Find each WBC.
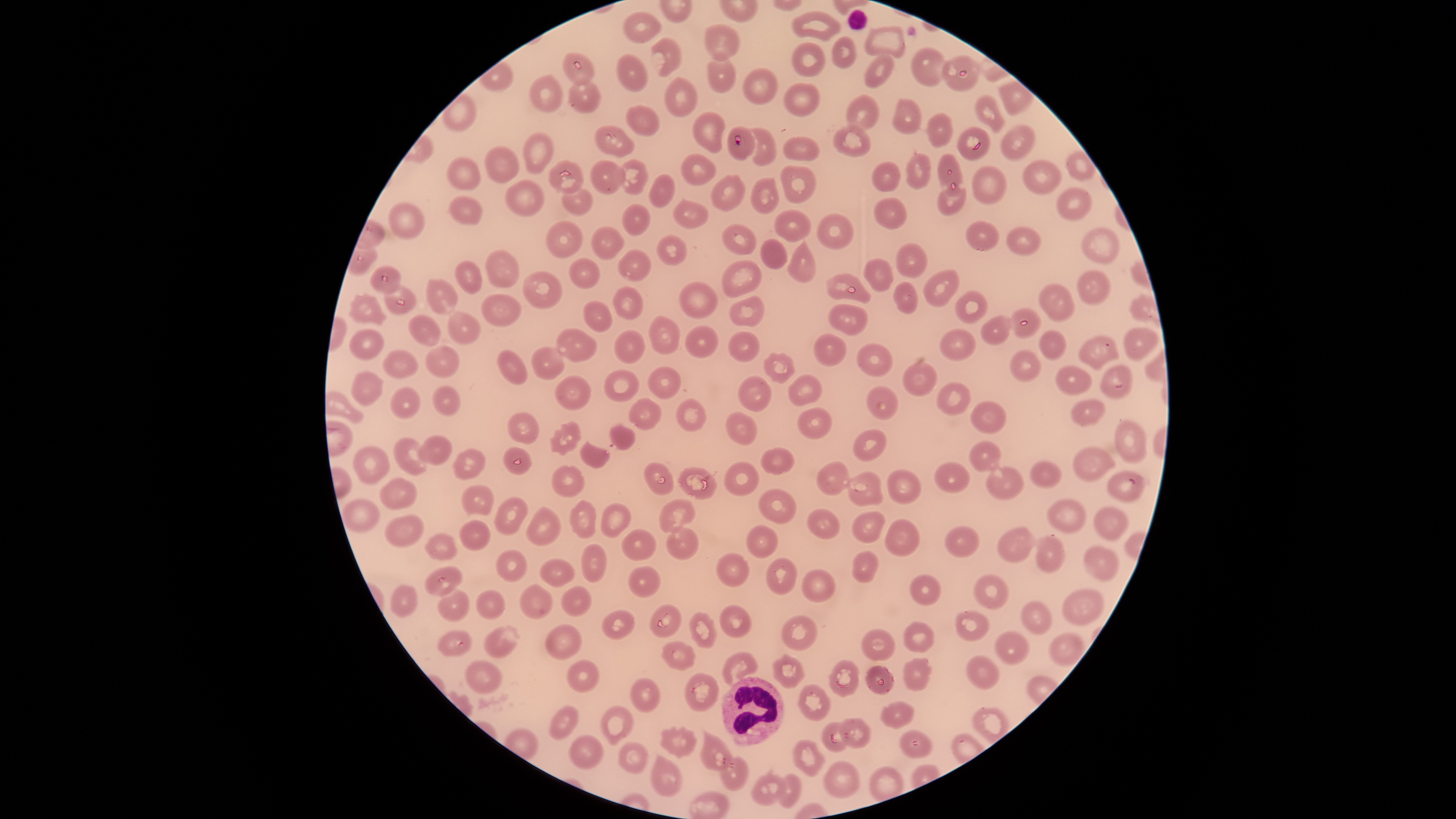
Approximate bounding boxes, in pixels from the top-left corner.
WBCs: (left=722, top=676, right=784, bottom=745).

image size = 1456×819 pixels
capture = smartphone photograph through the microscope eyepiece
parasitized RBCs = approximate bounding boxes, in pixels from the top-left corner: (left=727, top=126, right=756, bottom=161)
stain = Giemsa
presence = malaria parasites identified
species = Plasmodium falciparum
uninfected RBCs = approximate bounding boxes, in pixels from the top-left corner: (left=791, top=10, right=842, bottom=42), (left=622, top=11, right=663, bottom=44), (left=704, top=23, right=741, bottom=62), (left=864, top=24, right=907, bottom=59), (left=831, top=35, right=857, bottom=69), (left=650, top=36, right=683, bottom=77), (left=791, top=42, right=825, bottom=76), (left=909, top=46, right=947, bottom=87), (left=705, top=47, right=736, bottom=93), (left=562, top=51, right=596, bottom=87), (left=863, top=52, right=895, bottom=87), (left=616, top=53, right=649, bottom=92), (left=942, top=54, right=980, bottom=92), (left=742, top=67, right=778, bottom=105), (left=529, top=74, right=565, bottom=113), (left=664, top=77, right=698, bottom=117), (left=568, top=78, right=602, bottom=114), (left=782, top=81, right=821, bottom=117), (left=846, top=94, right=880, bottom=131), (left=974, top=94, right=1005, bottom=134), (left=891, top=98, right=922, bottom=133), (left=624, top=104, right=660, bottom=138), (left=691, top=111, right=725, bottom=153), (left=927, top=113, right=954, bottom=148), (left=832, top=122, right=873, bottom=157), (left=594, top=124, right=635, bottom=157), (left=1000, top=124, right=1037, bottom=161), (left=749, top=127, right=778, bottom=166), (left=957, top=127, right=991, bottom=160), (left=522, top=131, right=554, bottom=175), (left=782, top=136, right=820, bottom=162), (left=485, top=144, right=519, bottom=184), (left=1064, top=150, right=1097, bottom=183), (left=680, top=152, right=718, bottom=187), (left=904, top=152, right=932, bottom=190), (left=938, top=152, right=964, bottom=197), (left=447, top=157, right=481, bottom=191), (left=618, top=158, right=648, bottom=195), (left=548, top=159, right=585, bottom=194), (left=1021, top=159, right=1062, bottom=195), (left=588, top=160, right=626, bottom=195), (left=871, top=160, right=902, bottom=194), (left=780, top=164, right=818, bottom=203), (left=970, top=166, right=1008, bottom=205), (left=648, top=172, right=676, bottom=208), (left=710, top=173, right=745, bottom=212), (left=749, top=177, right=779, bottom=214), (left=504, top=179, right=545, bottom=216), (left=935, top=183, right=967, bottom=218), (left=1055, top=186, right=1091, bottom=221), (left=561, top=187, right=594, bottom=216), (left=448, top=195, right=485, bottom=225), (left=873, top=196, right=908, bottom=229), (left=672, top=197, right=708, bottom=230), (left=387, top=201, right=427, bottom=241), (left=621, top=203, right=651, bottom=236), (left=774, top=208, right=811, bottom=243), (left=816, top=213, right=854, bottom=250), (left=965, top=220, right=1000, bottom=252), (left=545, top=221, right=583, bottom=259), (left=722, top=224, right=757, bottom=255), (left=591, top=226, right=626, bottom=261), (left=1006, top=226, right=1041, bottom=257), (left=1080, top=227, right=1120, bottom=265), (left=656, top=236, right=688, bottom=267), (left=786, top=237, right=817, bottom=282), (left=759, top=238, right=788, bottom=269), (left=896, top=241, right=928, bottom=278), (left=485, top=249, right=521, bottom=290), (left=617, top=250, right=653, bottom=282), (left=569, top=258, right=600, bottom=289), (left=862, top=258, right=894, bottom=293), (left=720, top=259, right=763, bottom=298), (left=455, top=261, right=482, bottom=294), (left=369, top=266, right=401, bottom=295), (left=922, top=268, right=961, bottom=308), (left=1075, top=270, right=1111, bottom=306), (left=522, top=271, right=563, bottom=309), (left=824, top=272, right=872, bottom=304), (left=426, top=278, right=459, bottom=315), (left=892, top=280, right=918, bottom=314), (left=678, top=281, right=721, bottom=320), (left=1037, top=282, right=1075, bottom=323), (left=384, top=285, right=417, bottom=316), (left=611, top=285, right=644, bottom=320), (left=954, top=290, right=986, bottom=325), (left=349, top=293, right=387, bottom=326), (left=481, top=293, right=522, bottom=327), (left=729, top=295, right=765, bottom=326), (left=583, top=300, right=614, bottom=332), (left=827, top=303, right=868, bottom=336), (left=1010, top=307, right=1042, bottom=340), (left=446, top=310, right=483, bottom=345), (left=407, top=314, right=442, bottom=348), (left=648, top=315, right=682, bottom=355), (left=979, top=315, right=1011, bottom=347), (left=685, top=324, right=720, bottom=358), (left=1123, top=325, right=1159, bottom=361), (left=555, top=326, right=599, bottom=362), (left=938, top=327, right=977, bottom=362), (left=348, top=328, right=385, bottom=361), (left=613, top=329, right=645, bottom=363), (left=1038, top=329, right=1066, bottom=361), (left=727, top=330, right=762, bottom=363), (left=813, top=332, right=849, bottom=366), (left=1077, top=334, right=1120, bottom=372), (left=855, top=342, right=894, bottom=377), (left=424, top=343, right=460, bottom=380), (left=530, top=346, right=566, bottom=381), (left=495, top=348, right=529, bottom=387), (left=381, top=349, right=419, bottom=380), (left=1009, top=350, right=1042, bottom=383), (left=763, top=351, right=797, bottom=384), (left=901, top=360, right=937, bottom=396), (left=1054, top=364, right=1092, bottom=396), (left=1099, top=364, right=1134, bottom=399), (left=648, top=366, right=680, bottom=400), (left=350, top=370, right=384, bottom=408), (left=603, top=370, right=639, bottom=402), (left=788, top=374, right=824, bottom=408), (left=555, top=375, right=591, bottom=410), (left=738, top=375, right=773, bottom=412), (left=936, top=382, right=973, bottom=416), (left=865, top=384, right=899, bottom=422), (left=432, top=385, right=462, bottom=417), (left=389, top=386, right=421, bottom=420), (left=675, top=397, right=706, bottom=432), (left=628, top=398, right=663, bottom=432), (left=1070, top=398, right=1107, bottom=427), (left=970, top=400, right=1008, bottom=434), (left=797, top=406, right=833, bottom=439), (left=507, top=411, right=539, bottom=445), (left=725, top=411, right=758, bottom=446), (left=1115, top=418, right=1147, bottom=465), (left=549, top=421, right=583, bottom=456), (left=609, top=423, right=638, bottom=452), (left=852, top=429, right=888, bottom=462), (left=417, top=435, right=453, bottom=466), (left=392, top=437, right=428, bottom=477), (left=579, top=440, right=610, bottom=469), (left=968, top=440, right=1001, bottom=473), (left=1072, top=445, right=1116, bottom=482), (left=503, top=446, right=533, bottom=475), (left=352, top=447, right=392, bottom=486), (left=760, top=447, right=796, bottom=475), (left=453, top=449, right=486, bottom=481), (left=1029, top=460, right=1062, bottom=489), (left=643, top=461, right=674, bottom=497), (left=724, top=461, right=761, bottom=498), (left=816, top=461, right=850, bottom=496), (left=932, top=461, right=970, bottom=494), (left=551, top=465, right=586, bottom=498), (left=985, top=465, right=1025, bottom=501), (left=677, top=466, right=719, bottom=501), (left=886, top=469, right=922, bottom=504), (left=1106, top=469, right=1148, bottom=504), (left=846, top=470, right=884, bottom=507), (left=380, top=477, right=418, bottom=511), (left=461, top=485, right=494, bottom=517), (left=757, top=487, right=797, bottom=525), (left=493, top=497, right=528, bottom=536), (left=1046, top=497, right=1089, bottom=535), (left=340, top=498, right=382, bottom=534), (left=569, top=499, right=599, bottom=540), (left=658, top=499, right=698, bottom=534), (left=601, top=503, right=632, bottom=539), (left=525, top=506, right=562, bottom=547), (left=1093, top=506, right=1129, bottom=543), (left=807, top=508, right=841, bottom=540), (left=851, top=512, right=887, bottom=543), (left=384, top=514, right=426, bottom=549), (left=884, top=518, right=920, bottom=557), (left=459, top=520, right=493, bottom=551), (left=746, top=524, right=779, bottom=559), (left=944, top=525, right=981, bottom=558), (left=666, top=526, right=700, bottom=562), (left=996, top=526, right=1036, bottom=563), (left=620, top=528, right=658, bottom=563), (left=425, top=531, right=457, bottom=561), (left=1035, top=534, right=1067, bottom=575), (left=581, top=543, right=609, bottom=585), (left=1083, top=545, right=1119, bottom=581), (left=496, top=549, right=529, bottom=583), (left=852, top=549, right=879, bottom=583), (left=716, top=551, right=751, bottom=589), (left=765, top=556, right=798, bottom=597), (left=540, top=558, right=575, bottom=588), (left=628, top=564, right=662, bottom=599), (left=424, top=566, right=463, bottom=596), (left=800, top=568, right=839, bottom=604), (left=910, top=574, right=943, bottom=607), (left=973, top=574, right=1010, bottom=610), (left=520, top=583, right=554, bottom=620), (left=390, top=584, right=418, bottom=620), (left=561, top=584, right=592, bottom=617), (left=436, top=586, right=471, bottom=622), (left=1061, top=587, right=1106, bottom=627), (left=475, top=588, right=507, bottom=620), (left=1020, top=600, right=1053, bottom=636), (left=649, top=603, right=682, bottom=638), (left=718, top=604, right=754, bottom=639), (left=955, top=608, right=991, bottom=642), (left=602, top=610, right=637, bottom=640), (left=687, top=611, right=718, bottom=649), (left=780, top=614, right=817, bottom=653), (left=903, top=620, right=936, bottom=653), (left=545, top=624, right=584, bottom=662), (left=483, top=625, right=521, bottom=659), (left=860, top=627, right=898, bottom=662), (left=436, top=629, right=473, bottom=658), (left=994, top=630, right=1029, bottom=666), (left=1049, top=632, right=1085, bottom=667), (left=660, top=640, right=696, bottom=670), (left=721, top=652, right=759, bottom=685), (left=772, top=653, right=806, bottom=689), (left=965, top=655, right=1001, bottom=690), (left=464, top=658, right=503, bottom=694), (left=827, top=658, right=860, bottom=697), (left=902, top=658, right=934, bottom=692), (left=566, top=659, right=601, bottom=693), (left=864, top=666, right=896, bottom=695), (left=684, top=672, right=720, bottom=712), (left=629, top=678, right=661, bottom=712), (left=798, top=684, right=830, bottom=721), (left=880, top=701, right=915, bottom=728), (left=548, top=705, right=581, bottom=741), (left=600, top=705, right=635, bottom=746), (left=838, top=717, right=872, bottom=748), (left=821, top=721, right=850, bottom=751), (left=660, top=726, right=698, bottom=760), (left=700, top=729, right=734, bottom=771), (left=899, top=729, right=933, bottom=759), (left=568, top=735, right=605, bottom=770), (left=792, top=738, right=825, bottom=779), (left=618, top=742, right=649, bottom=774), (left=649, top=753, right=683, bottom=797), (left=721, top=756, right=750, bottom=791), (left=822, top=760, right=859, bottom=799), (left=752, top=772, right=787, bottom=806), (left=777, top=773, right=803, bottom=808)
preparation = thin smear of blood
field of view = single
visible region = circular